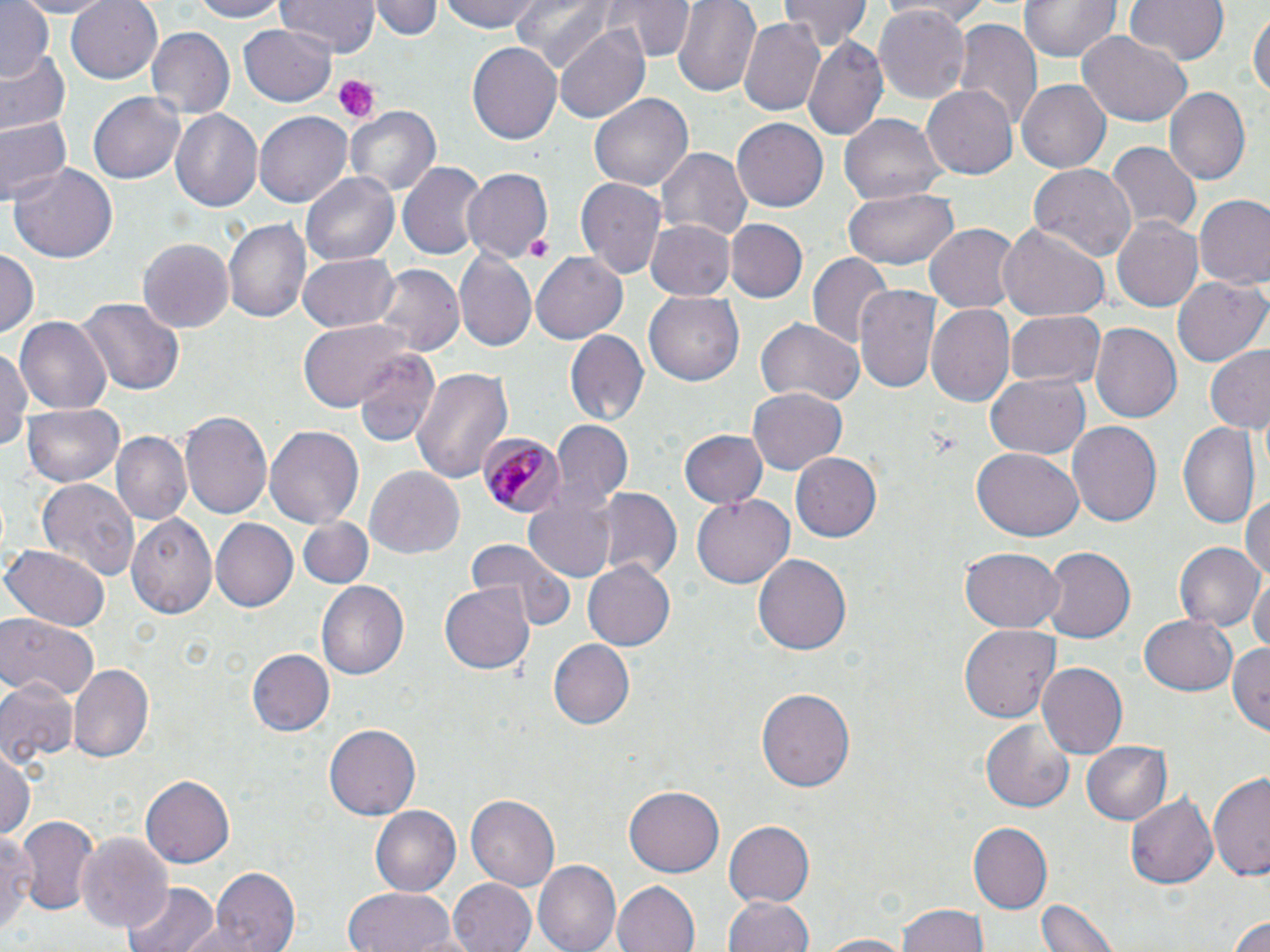

slide_level_diagnosis: Plasmodium malariae
uninfected_red_blood_cell_locations: 'approximate bounding boxes as [x1, y1, x2, y2] in pixels: [0, 0, 53, 80], [10, 0, 124, 17], [65, 0, 164, 84], [190, 0, 283, 22], [278, 0, 378, 57], [375, 0, 441, 42], [442, 0, 544, 33], [512, 0, 616, 76], [609, 0, 692, 63], [671, 0, 761, 95], [883, 0, 1003, 22], [1019, 0, 1120, 64], [1123, 0, 1231, 66], [777, 1, 870, 52], [874, 4, 973, 103], [1250, 9, 1269, 106], [739, 18, 825, 114], [951, 21, 1040, 133], [239, 25, 338, 105], [554, 25, 650, 123], [146, 27, 236, 117], [1076, 29, 1190, 125], [803, 34, 887, 140], [468, 41, 562, 146], [0, 49, 71, 139], [1017, 80, 1111, 174], [924, 84, 1019, 179], [1166, 87, 1253, 185], [589, 91, 692, 189], [89, 92, 184, 185], [346, 106, 438, 198], [168, 107, 263, 211], [256, 112, 354, 207], [840, 114, 946, 206], [0, 116, 69, 203], [734, 117, 828, 212], [1106, 141, 1198, 231], [655, 144, 751, 240], [397, 160, 484, 261], [10, 162, 118, 264], [1027, 164, 1138, 263], [464, 168, 557, 262], [301, 170, 403, 266], [575, 178, 668, 282], [841, 189, 959, 270], [1193, 196, 1270, 292], [1113, 217, 1203, 312], [645, 218, 736, 300], [224, 220, 309, 322], [727, 220, 807, 301], [999, 222, 1111, 322], [926, 224, 1021, 313], [137, 235, 233, 331], [0, 249, 38, 339], [530, 252, 628, 344], [455, 253, 536, 351], [807, 253, 892, 349], [295, 254, 401, 335], [373, 265, 463, 358], [1173, 276, 1267, 366], [853, 282, 941, 397], [643, 293, 744, 387], [77, 295, 182, 399], [927, 304, 1014, 406], [1004, 309, 1105, 389], [16, 317, 110, 413], [297, 320, 412, 411], [757, 320, 864, 406], [1088, 323, 1181, 427], [566, 331, 649, 425], [0, 343, 30, 459], [1204, 346, 1270, 435], [353, 348, 441, 447], [410, 367, 514, 484], [985, 374, 1090, 460], [748, 386, 847, 475], [21, 401, 125, 485], [179, 410, 273, 519], [549, 418, 632, 514], [1068, 421, 1163, 529], [1178, 421, 1260, 530], [264, 424, 364, 530], [678, 428, 767, 508], [109, 431, 191, 526], [972, 445, 1082, 541], [789, 452, 880, 542], [366, 466, 464, 560], [35, 477, 141, 582], [588, 487, 682, 582], [1244, 490, 1270, 590], [693, 494, 793, 588], [521, 500, 615, 583], [126, 510, 215, 619], [212, 517, 300, 612], [297, 517, 372, 590], [465, 538, 576, 630], [1173, 542, 1261, 633], [1, 544, 110, 630], [960, 548, 1063, 631], [1039, 548, 1134, 646], [754, 554, 851, 658], [583, 560, 675, 651], [1250, 573, 1270, 661], [316, 580, 408, 682], [439, 582, 534, 675], [1140, 612, 1238, 696], [0, 615, 98, 700], [960, 624, 1060, 722], [549, 640, 634, 728], [1229, 640, 1270, 736], [246, 648, 334, 737], [69, 663, 154, 761], [1038, 663, 1129, 758], [0, 676, 78, 768], [757, 686, 854, 794], [981, 720, 1074, 814], [324, 724, 420, 821], [1082, 741, 1169, 825], [0, 747, 36, 841], [1209, 771, 1270, 880], [140, 774, 235, 868], [624, 785, 725, 877], [1128, 793, 1218, 888], [466, 794, 560, 890], [370, 805, 461, 896], [12, 814, 98, 912], [723, 819, 815, 908], [967, 822, 1052, 913], [1, 827, 34, 940], [74, 832, 173, 936], [534, 861, 621, 952], [208, 867, 299, 951], [448, 877, 538, 952], [612, 880, 702, 952], [124, 881, 219, 952], [342, 885, 459, 952], [725, 895, 816, 952], [1039, 895, 1119, 952], [899, 906, 988, 952], [1226, 909, 1270, 952], [812, 932, 920, 951]'
plasmodium_malariae_infected_red_blood_cell_locations: 'approximate bounding boxes as [x1, y1, x2, y2] in pixels: [480, 431, 564, 518]'
modality: light microscopy
field_of_view: one of a larger specimen
magnification: 1000x
platelet_locations: 'approximate bounding boxes as [x1, y1, x2, y2] in pixels: [334, 77, 376, 123], [522, 231, 552, 264]'
image_size: 1270×952 pixels
preparation: thin blood film
stain: May-Grünwald-Giemsa